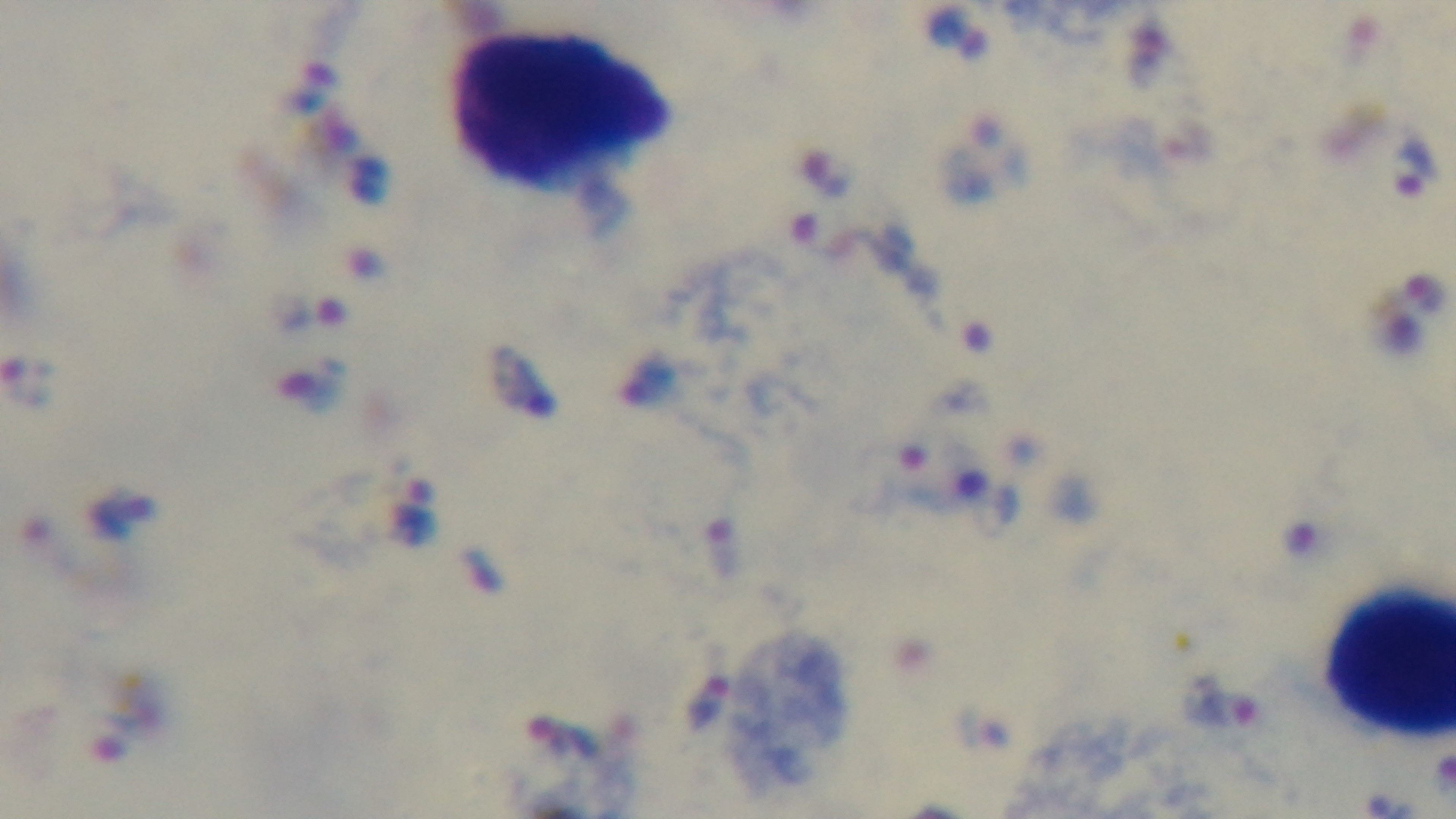
Captured with a mounted 4K digital camera. Light microscopy. Preparation: thick. Giemsa stain. Malaria status: infected. Single field of view. Oil-immersion objective, 100x.